Report the malaria status of this cell.
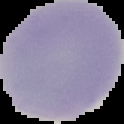

Uninfected.

image size = 124×124 pixels
preparation = thin blood smear
image type = segmented cell region on a black background